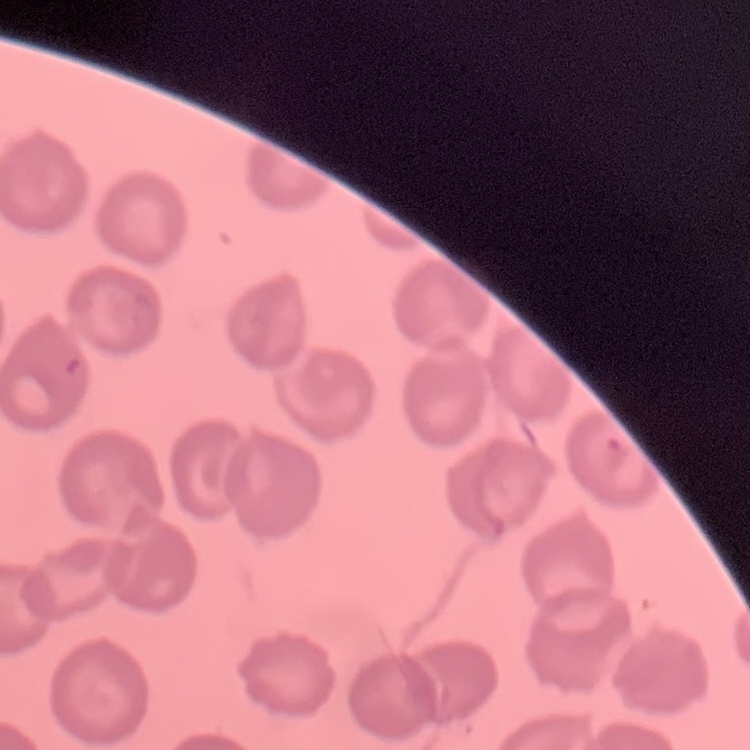

erythrocyte morphology = no rouleaux formation
stain = Field's or Giemsa
preparation = thin blood film
image type = one tile cut from a larger photomicrograph